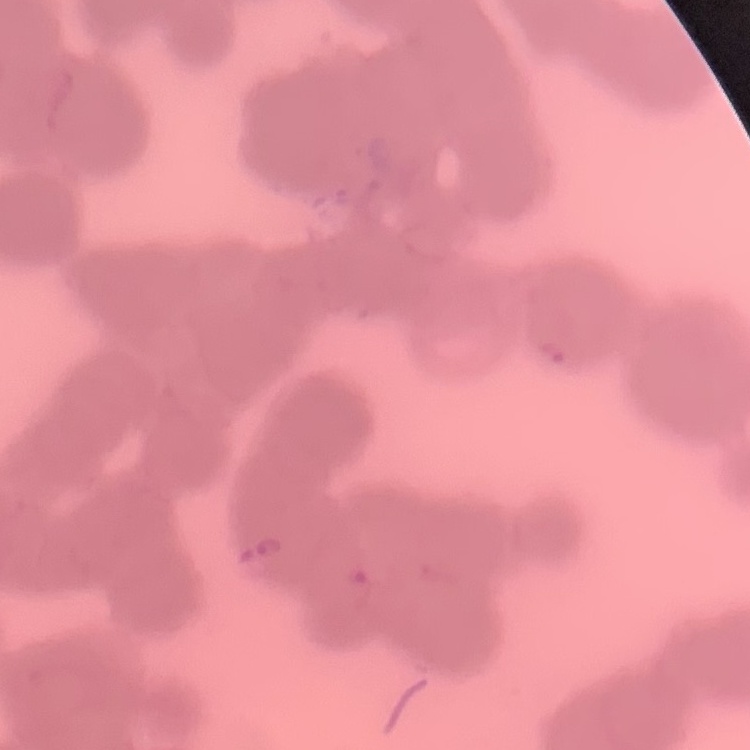
erythrocyte morphology = rouleaux formation
stain = Field's or Giemsa
preparation = thin blood film
image type = square crop of a larger photomicrograph